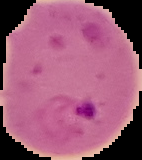

image size = 142×160 pixels
malaria status = parasitized
image type = segmented cell region with the area outside set to black
preparation = thin blood smear